Report the malaria status of this cell.
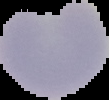
Parasitized.

{
  "image_size": "109×100 pixels",
  "image_type": "segmented cell region with the area outside set to black",
  "preparation": "thin blood smear"
}